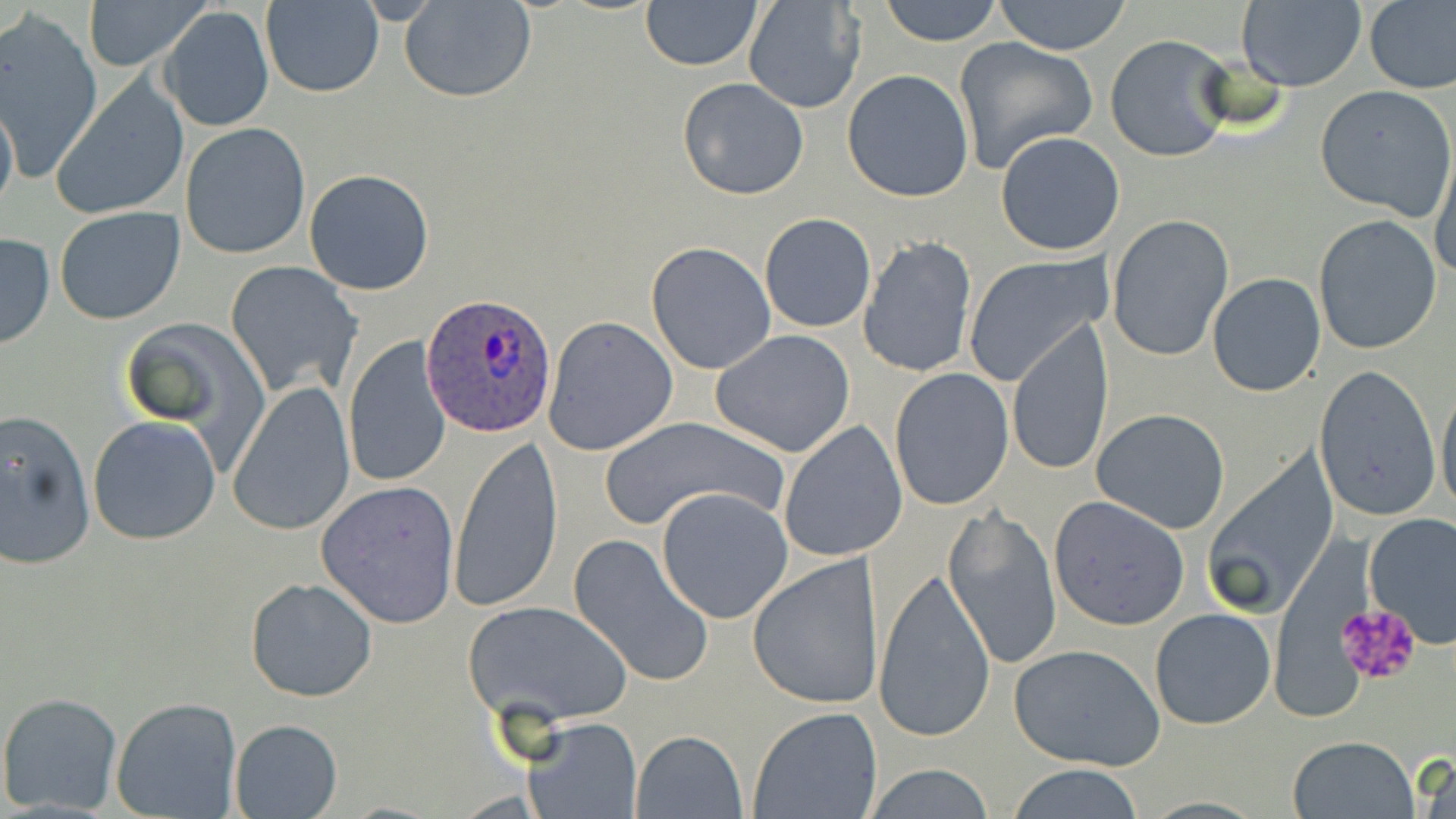

Approximate bounding boxes as (x1, y1, x2, y2) in pixels. Plasmodium ovale-infected red blood cell locations: (421, 293, 556, 438). Platelet locations: (1335, 600, 1421, 687). Uninfected red blood cell locations: (80, 0, 211, 71), (399, 0, 537, 104), (640, 0, 761, 71), (879, 0, 1004, 46), (993, 0, 1133, 54), (1363, 0, 1456, 94), (741, 1, 866, 114), (1236, 1, 1367, 92), (260, 2, 384, 98), (159, 7, 274, 132), (0, 13, 103, 180), (1104, 33, 1236, 162), (953, 37, 1098, 176), (842, 70, 974, 202), (677, 77, 809, 200), (51, 79, 187, 219), (1316, 85, 1455, 220), (0, 93, 18, 223), (180, 123, 311, 260), (995, 130, 1126, 257), (1432, 147, 1456, 285), (304, 169, 436, 296), (53, 206, 186, 325), (758, 212, 877, 333), (1107, 213, 1234, 361), (1312, 215, 1443, 355), (0, 232, 53, 350), (858, 235, 978, 379), (647, 241, 777, 375), (964, 252, 1111, 386), (225, 260, 363, 399), (1207, 271, 1326, 396), (541, 315, 678, 456), (121, 319, 269, 462), (1006, 319, 1114, 477), (710, 330, 855, 457), (343, 335, 450, 488), (1314, 364, 1440, 522), (889, 367, 1014, 510), (1437, 378, 1456, 522), (227, 381, 356, 537), (1091, 408, 1232, 534), (0, 409, 96, 572), (598, 413, 787, 533), (88, 414, 222, 544), (778, 422, 907, 563), (447, 436, 561, 616), (1201, 449, 1339, 621), (317, 481, 461, 627), (654, 486, 792, 624), (1048, 495, 1190, 630), (942, 505, 1062, 669), (1363, 512, 1456, 646), (569, 534, 716, 690), (747, 554, 884, 710), (873, 567, 997, 743), (245, 576, 379, 703), (462, 599, 632, 727), (1150, 608, 1276, 730), (1009, 643, 1166, 771), (0, 691, 125, 814), (111, 697, 242, 819), (749, 708, 881, 819), (519, 716, 641, 819), (229, 718, 342, 819), (630, 730, 746, 818), (1285, 734, 1420, 819), (1415, 755, 1456, 819), (860, 763, 998, 819), (1003, 763, 1149, 819). Slide-level diagnosis: Plasmodium ovale. Image is 1456×819 pixels. Captured at 1000x magnification. Optical microscopy. Single field of view. Thin blood film. May-Grünwald-Giemsa-stained preparation.